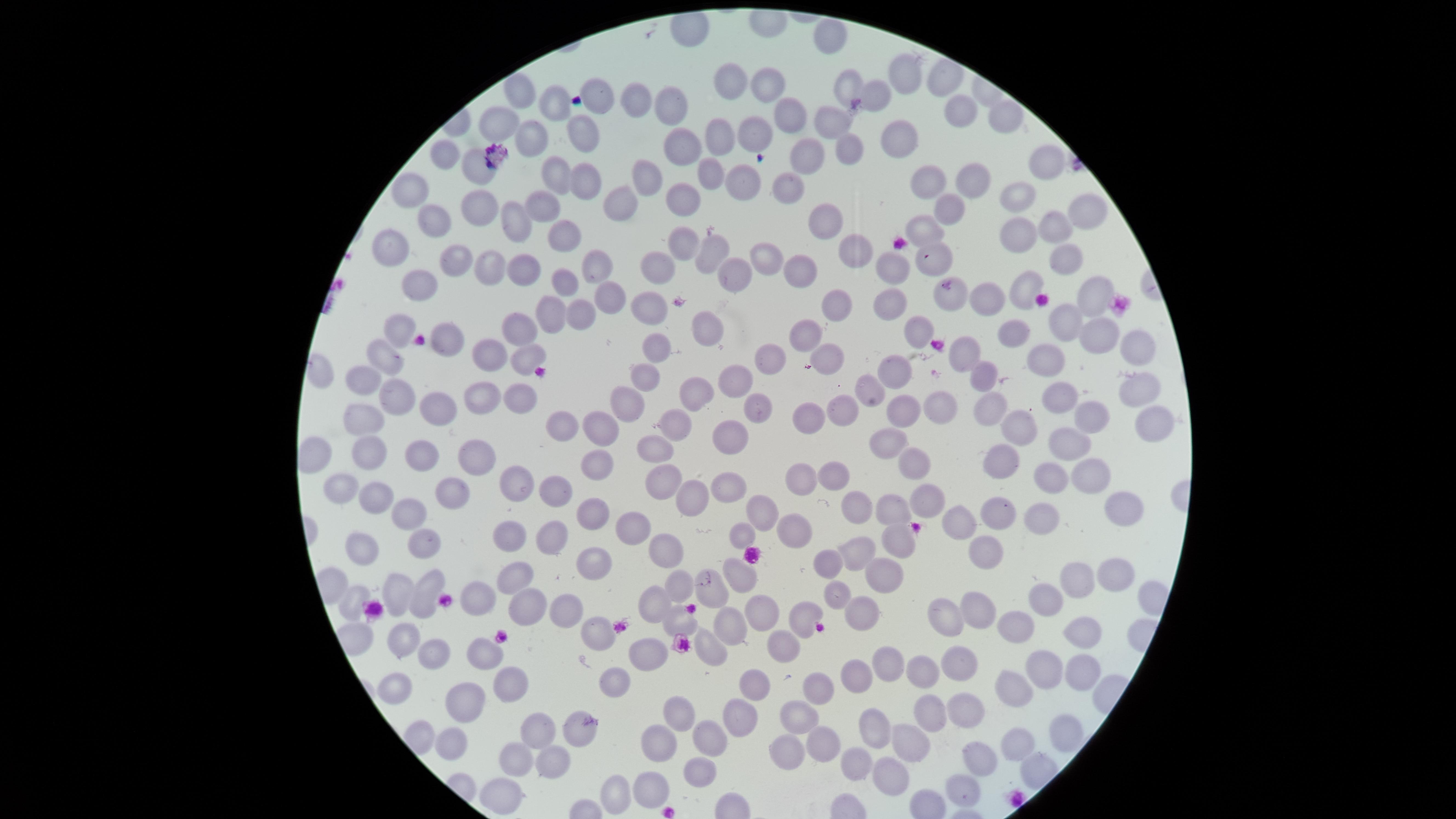
capture = smartphone photograph through the microscope eyepiece
image size = 1456×819 pixels
uninfected red blood cells = approximate marker points, in pixels from the top-left corner: (x=827, y=34), (x=908, y=69), (x=939, y=76), (x=765, y=80), (x=729, y=82), (x=849, y=83), (x=521, y=89), (x=881, y=91), (x=601, y=96), (x=669, y=98), (x=635, y=102), (x=551, y=108), (x=785, y=114), (x=961, y=115), (x=500, y=119), (x=1002, y=119), (x=837, y=120), (x=578, y=129), (x=902, y=135), (x=725, y=136), (x=756, y=137), (x=525, y=138), (x=843, y=141), (x=681, y=146), (x=798, y=148), (x=450, y=156), (x=1040, y=162), (x=709, y=168), (x=477, y=169), (x=558, y=173), (x=652, y=177), (x=787, y=180), (x=744, y=181), (x=929, y=181), (x=588, y=183), (x=974, y=185), (x=410, y=190), (x=682, y=198), (x=1021, y=198), (x=540, y=203), (x=480, y=204), (x=628, y=206), (x=1087, y=206), (x=947, y=207), (x=440, y=215), (x=823, y=215), (x=515, y=225), (x=1052, y=227), (x=931, y=232), (x=556, y=234), (x=1019, y=235), (x=393, y=239), (x=681, y=240), (x=850, y=246), (x=711, y=247), (x=460, y=251), (x=931, y=252), (x=769, y=254), (x=1070, y=254), (x=597, y=258), (x=663, y=265), (x=897, y=265), (x=492, y=268), (x=525, y=269), (x=798, y=269), (x=735, y=279), (x=1025, y=281), (x=415, y=285), (x=566, y=285), (x=606, y=293), (x=1095, y=294), (x=979, y=295), (x=951, y=297), (x=834, y=298), (x=890, y=298), (x=654, y=303), (x=583, y=312), (x=552, y=314), (x=712, y=323), (x=1069, y=324), (x=406, y=327), (x=518, y=331), (x=1094, y=332), (x=1015, y=334), (x=806, y=335), (x=910, y=335), (x=449, y=341), (x=1131, y=343), (x=654, y=350), (x=968, y=352), (x=388, y=354), (x=826, y=357), (x=522, y=359), (x=1061, y=359), (x=490, y=360), (x=775, y=361), (x=899, y=371), (x=361, y=376), (x=735, y=377), (x=981, y=379), (x=645, y=381), (x=1143, y=383), (x=699, y=390), (x=870, y=391), (x=1061, y=394), (x=402, y=395), (x=479, y=397), (x=512, y=399), (x=748, y=400), (x=984, y=400), (x=628, y=402), (x=895, y=402), (x=927, y=403), (x=436, y=407), (x=842, y=407), (x=798, y=410), (x=1094, y=412), (x=369, y=414), (x=1163, y=417), (x=681, y=423), (x=560, y=427), (x=604, y=428), (x=1023, y=428), (x=731, y=431), (x=893, y=435), (x=1069, y=440), (x=365, y=444), (x=482, y=450), (x=665, y=450), (x=424, y=456), (x=1007, y=459), (x=916, y=460), (x=590, y=465), (x=1094, y=471), (x=836, y=472), (x=804, y=477), (x=1058, y=477), (x=667, y=478), (x=520, y=485), (x=448, y=491), (x=562, y=491), (x=348, y=494), (x=728, y=498), (x=922, y=498), (x=691, y=500), (x=377, y=505), (x=852, y=505), (x=1115, y=505), (x=895, y=510), (x=994, y=510), (x=766, y=512), (x=408, y=515), (x=955, y=518), (x=1035, y=519), (x=589, y=521), (x=635, y=523), (x=799, y=523), (x=744, y=531), (x=508, y=532), (x=548, y=535), (x=893, y=535), (x=424, y=541), (x=985, y=548), (x=368, y=552), (x=660, y=552), (x=852, y=552), (x=836, y=562), (x=591, y=564), (x=744, y=570), (x=877, y=573), (x=1109, y=573), (x=509, y=575), (x=1082, y=581), (x=681, y=582), (x=718, y=588), (x=399, y=594), (x=425, y=595), (x=837, y=596), (x=1050, y=597), (x=360, y=598), (x=515, y=600), (x=481, y=602), (x=654, y=602), (x=982, y=603), (x=756, y=604), (x=558, y=607), (x=862, y=608), (x=948, y=615), (x=806, y=617), (x=681, y=621), (x=727, y=623), (x=1019, y=629), (x=1077, y=631), (x=595, y=633), (x=410, y=641), (x=788, y=642), (x=714, y=650), (x=433, y=652), (x=640, y=652), (x=483, y=656), (x=956, y=659), (x=879, y=665), (x=1035, y=666), (x=924, y=671), (x=1069, y=671), (x=861, y=677), (x=616, y=680), (x=505, y=681), (x=752, y=684), (x=406, y=686), (x=824, y=688), (x=1012, y=692), (x=471, y=704), (x=969, y=710), (x=936, y=711), (x=682, y=715), (x=795, y=716), (x=741, y=717), (x=869, y=723), (x=582, y=725), (x=710, y=735), (x=1059, y=736), (x=454, y=737), (x=533, y=738), (x=906, y=742), (x=663, y=743), (x=1015, y=743), (x=829, y=744), (x=784, y=747), (x=523, y=758), (x=981, y=759), (x=860, y=760), (x=543, y=763), (x=699, y=768), (x=888, y=769), (x=652, y=781), (x=623, y=788), (x=962, y=790), (x=502, y=794)
presence = no malaria parasites identified
preparation = thin blood smear
stain = Giemsa
field of view = single
visible region = circular